Report the malaria status of this cell.
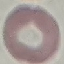
It is uninfected.

Summary:
  - Image type: automatically extracted cell patch, resized to 64 × 64 pixels
  - Stain: Giemsa
  - Preparation: thin blood film
  - Capture: smartphone through the microscope eyepiece